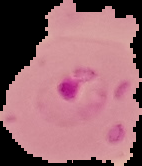

{
  "image_type": "segmented cell region with the area outside set to black",
  "preparation": "thin blood film",
  "result": "malaria parasites detected",
  "image_size": "142×166 pixels"
}